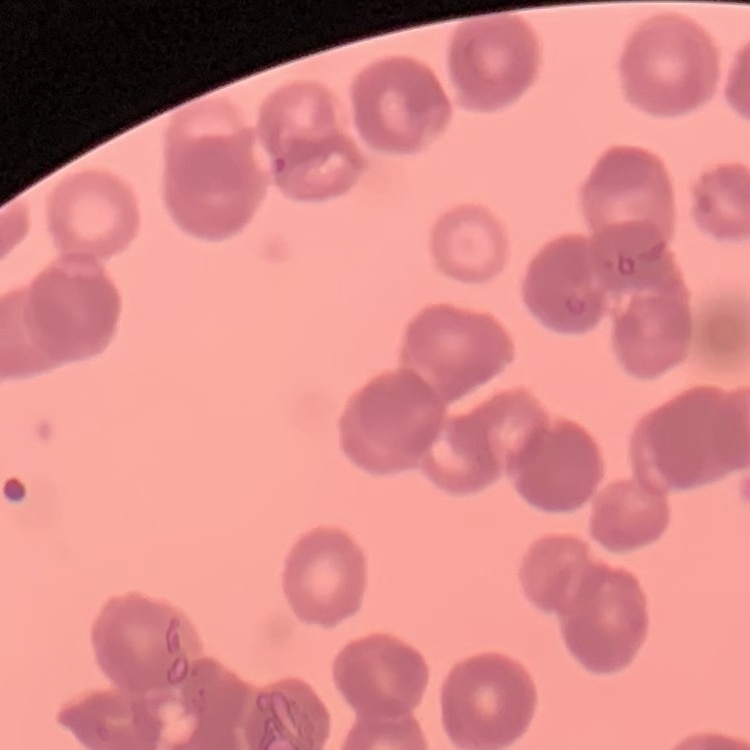

red blood cell morphology = rouleaux formation
image type = square crop of a larger photomicrograph
stain = Field's or Giemsa
preparation = thin blood smear